Report the malaria status of this cell.
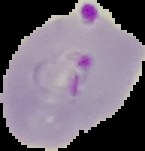

It is parasitized.

Segmented cell region on a black background. From a thin blood smear. Image is 145×151 pixels.